Point out each Plasmodium parasite.
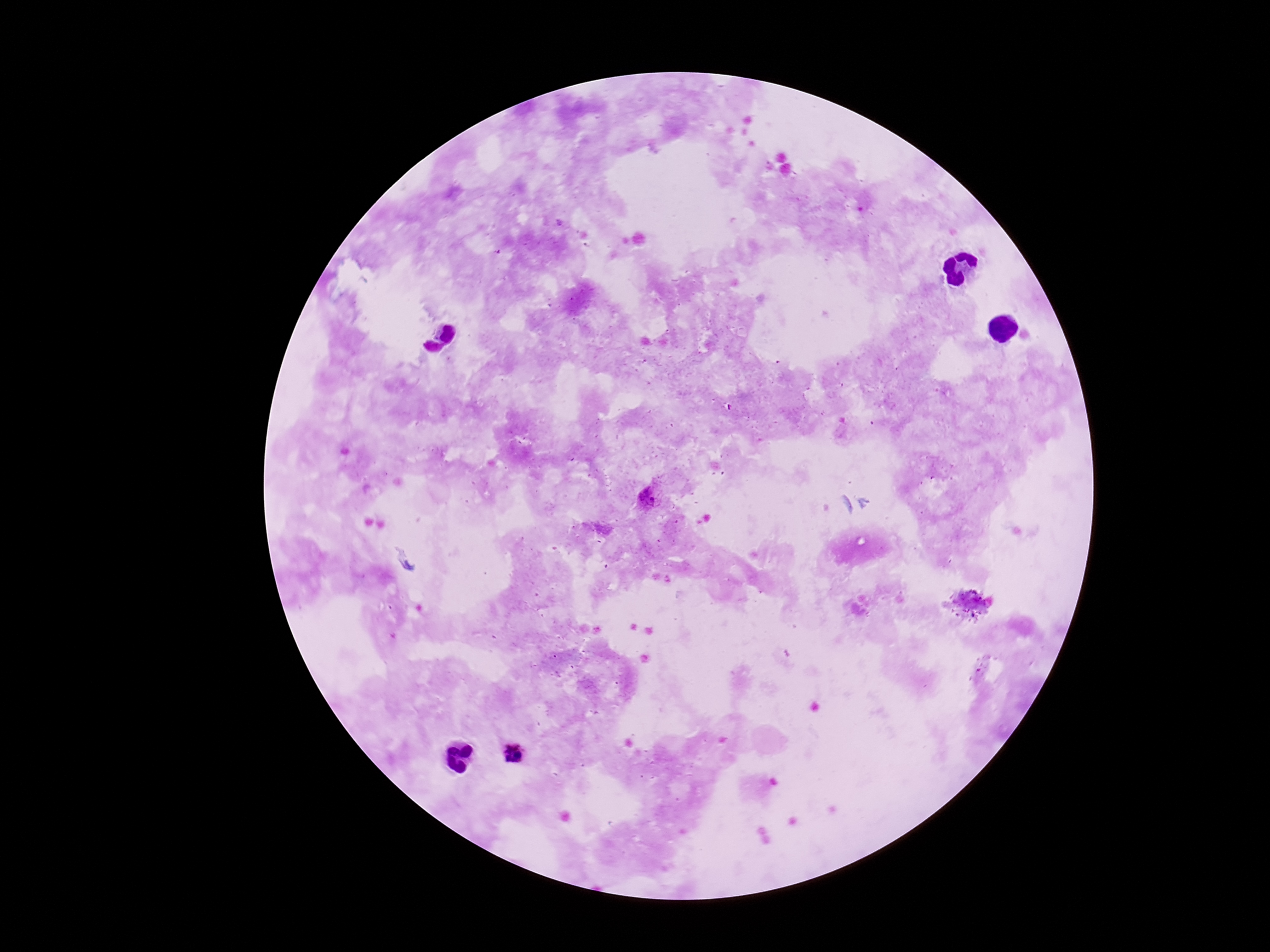

Approximate centers as {x, y} in pixels.
Plasmodium parasites: {651, 500}, {515, 751}.

Summary:
  - Field of view: one from this slide
  - Magnification: 100x
  - Preparation: thick blood film
  - Capture: smartphone camera through the microscope eyepiece
  - Stain: Giemsa
  - Patient malaria status: positive
  - Image size: 1270×952 pixels